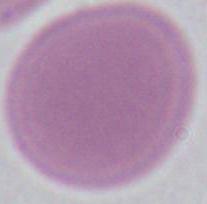
modality = photomicrograph
identification = red blood cell
magnification = 1000x